Comment on the morphology of the red blood cells.
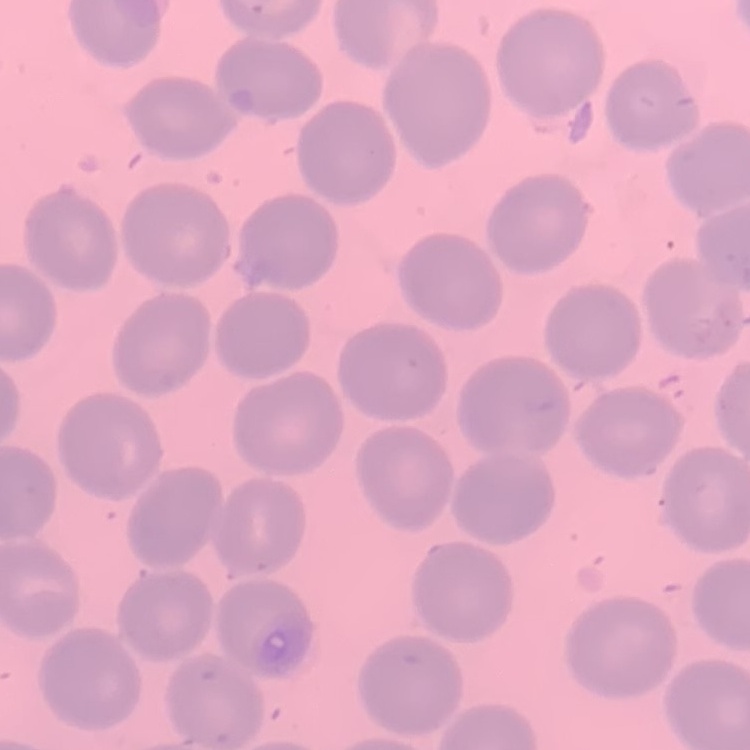

No rouleaux formation.

Summary:
  - Preparation: thin blood smear
  - Image type: square crop of a larger photomicrograph
  - Stain: Field's or Giemsa